Locate every malaria parasite by life-cycle stage, and every leukocyte.
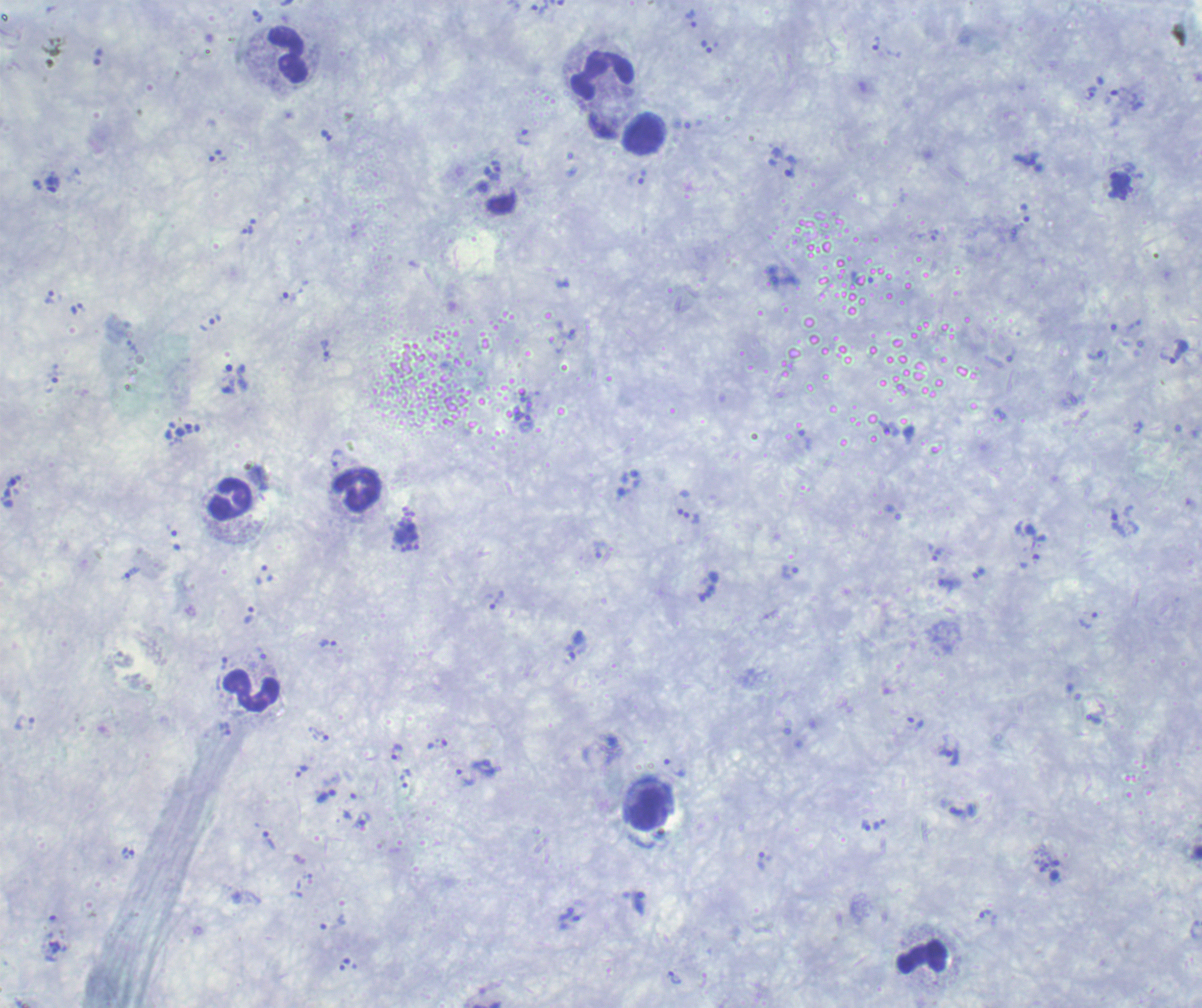
Approximate centers as {x, y} in pixels.
Trophozoites: {540, 9}, {257, 17}, {691, 19}, {876, 43}, {707, 47}, {1091, 93}, {327, 136}, {524, 138}, {790, 167}, {492, 170}, {641, 177}, {53, 184}, {248, 229}, {50, 297}, {290, 297}, {77, 308}, {215, 320}, {572, 334}, {326, 351}, {1095, 356}, {1168, 358}, {682, 501}, {692, 517}, {1118, 523}, {935, 552}, {132, 572}, {789, 572}, {978, 572}, {497, 599}, {1088, 620}, {328, 643}, {319, 736}, {945, 746}, {397, 752}, {675, 767}, {302, 772}, {465, 777}, {403, 781}, {958, 811}, {360, 822}, {866, 825}, {269, 841}, {128, 852}, {761, 862}, {1045, 868}, {984, 913}, {675, 977}.
Schizonts: {406, 537}.
No gametocyte forms observed.
Leukocytes: {289, 55}, {603, 74}, {645, 134}, {355, 491}, {230, 500}, {251, 690}, {648, 810}, {922, 956}.

{
  "magnification": "100x",
  "context": "previously used in a real diagnosis",
  "stain": "Romanowsky",
  "background_quality": "poor",
  "image_size": "1202×1008 pixels",
  "preparation": "thick blood film",
  "field_of_view": "one from this slide"
}